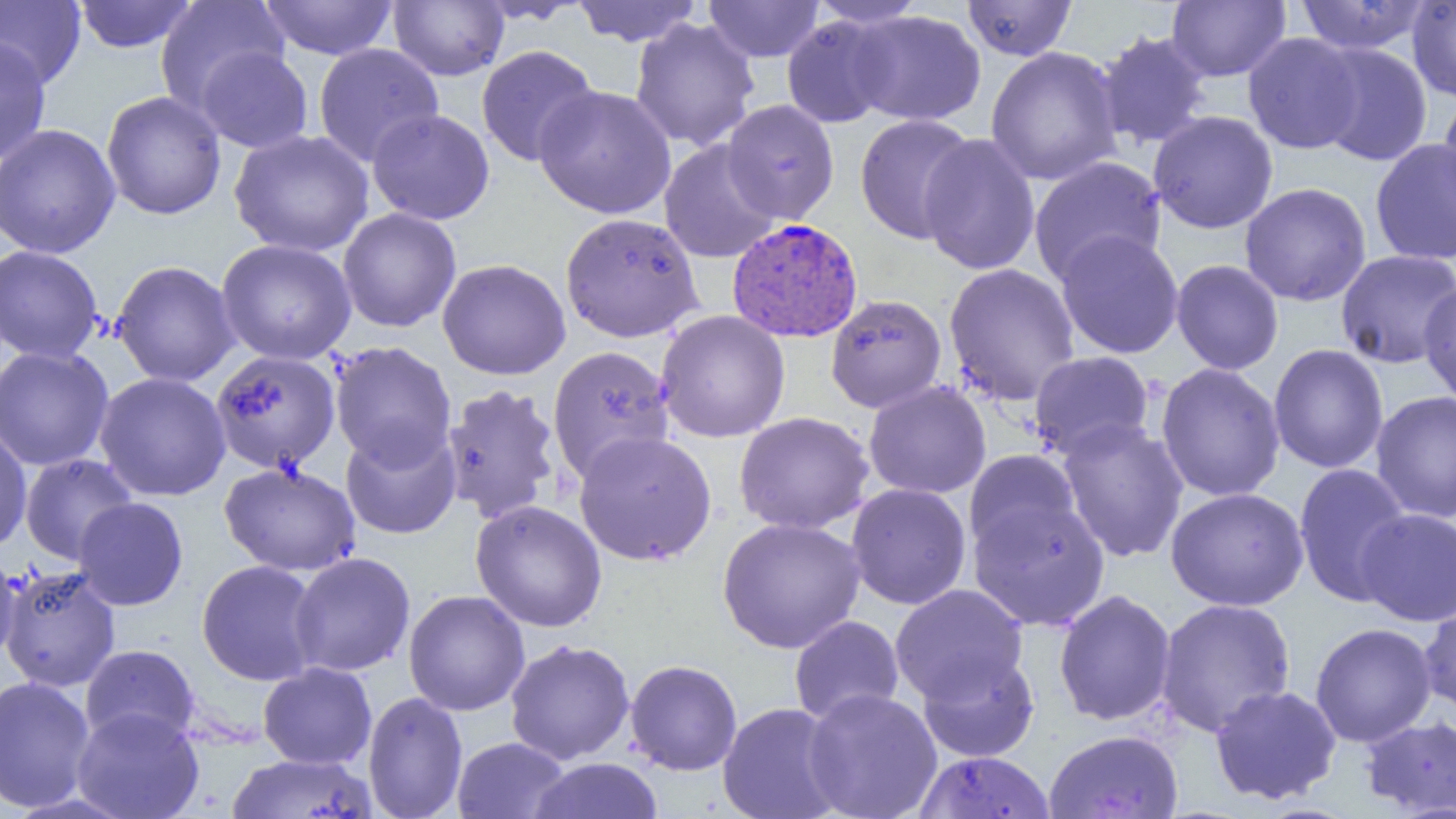
Approximate bounding boxes as (x1, y1, x2, y2) in pixels. Plasmodium vivax-infected red blood cell locations: (726, 217, 863, 343). Uninfected red blood cell locations: (72, 0, 199, 53), (259, 0, 399, 60), (806, 0, 929, 29), (961, 0, 1078, 61), (1294, 0, 1431, 55), (1407, 0, 1456, 102), (0, 1, 86, 88), (155, 1, 290, 115), (389, 1, 509, 81), (473, 1, 588, 25), (571, 1, 702, 46), (703, 1, 825, 63), (1167, 1, 1291, 82), (848, 9, 986, 126), (781, 14, 898, 129), (629, 17, 760, 152), (1094, 30, 1212, 150), (1243, 32, 1364, 154), (0, 35, 51, 165), (1311, 42, 1432, 166), (313, 43, 444, 167), (476, 45, 600, 167), (194, 46, 314, 154), (985, 46, 1123, 186), (534, 85, 676, 219), (1437, 90, 1456, 224), (101, 91, 226, 220), (721, 99, 839, 224), (367, 108, 495, 225), (1148, 110, 1279, 234), (854, 113, 978, 244), (0, 124, 121, 259), (229, 129, 374, 257), (918, 134, 1041, 275), (1369, 138, 1456, 267), (659, 140, 781, 264), (1028, 156, 1166, 285), (1239, 182, 1372, 307), (337, 208, 462, 333), (560, 212, 705, 343), (1055, 230, 1184, 359), (215, 239, 357, 365), (0, 245, 104, 363), (1335, 249, 1456, 369), (436, 258, 571, 380), (110, 260, 241, 387), (1170, 260, 1284, 375), (943, 262, 1081, 407), (1417, 279, 1456, 407), (825, 294, 947, 413), (655, 309, 791, 443), (330, 341, 457, 470), (1268, 343, 1389, 474), (0, 344, 115, 471), (547, 345, 676, 484), (210, 350, 342, 474), (1028, 350, 1155, 461), (1155, 362, 1286, 502), (93, 372, 231, 502), (863, 381, 992, 499), (439, 384, 563, 525), (1370, 391, 1456, 523), (733, 411, 875, 535), (1057, 418, 1190, 563), (340, 424, 462, 538), (0, 426, 33, 553), (573, 430, 718, 567), (964, 450, 1082, 557), (19, 453, 138, 565), (219, 461, 361, 576), (1293, 462, 1414, 606), (846, 483, 972, 610), (1165, 486, 1309, 611), (73, 497, 188, 610), (968, 497, 1110, 631), (469, 499, 608, 633), (1357, 508, 1455, 627), (716, 517, 866, 653), (0, 546, 22, 662), (288, 551, 416, 677), (196, 559, 323, 686), (1, 565, 121, 692), (890, 584, 1029, 705), (403, 589, 531, 716), (1053, 589, 1177, 727), (1155, 598, 1296, 737), (1419, 598, 1456, 718), (789, 615, 905, 726), (1309, 622, 1437, 748), (505, 638, 636, 765), (79, 644, 200, 748), (917, 649, 1040, 762), (624, 659, 743, 776), (257, 662, 377, 769), (0, 675, 97, 813), (1209, 684, 1342, 806), (802, 688, 943, 819), (363, 691, 468, 819), (718, 702, 845, 819), (71, 707, 205, 819), (1360, 714, 1456, 816), (1044, 729, 1183, 819), (451, 736, 571, 819), (915, 750, 1055, 819), (227, 753, 377, 818), (528, 757, 663, 819). Slide-level diagnosis: Plasmodium vivax. Thin blood smear. One field of a larger specimen. 1000x magnification. Image is 1456×819 pixels. Optical microscopy.